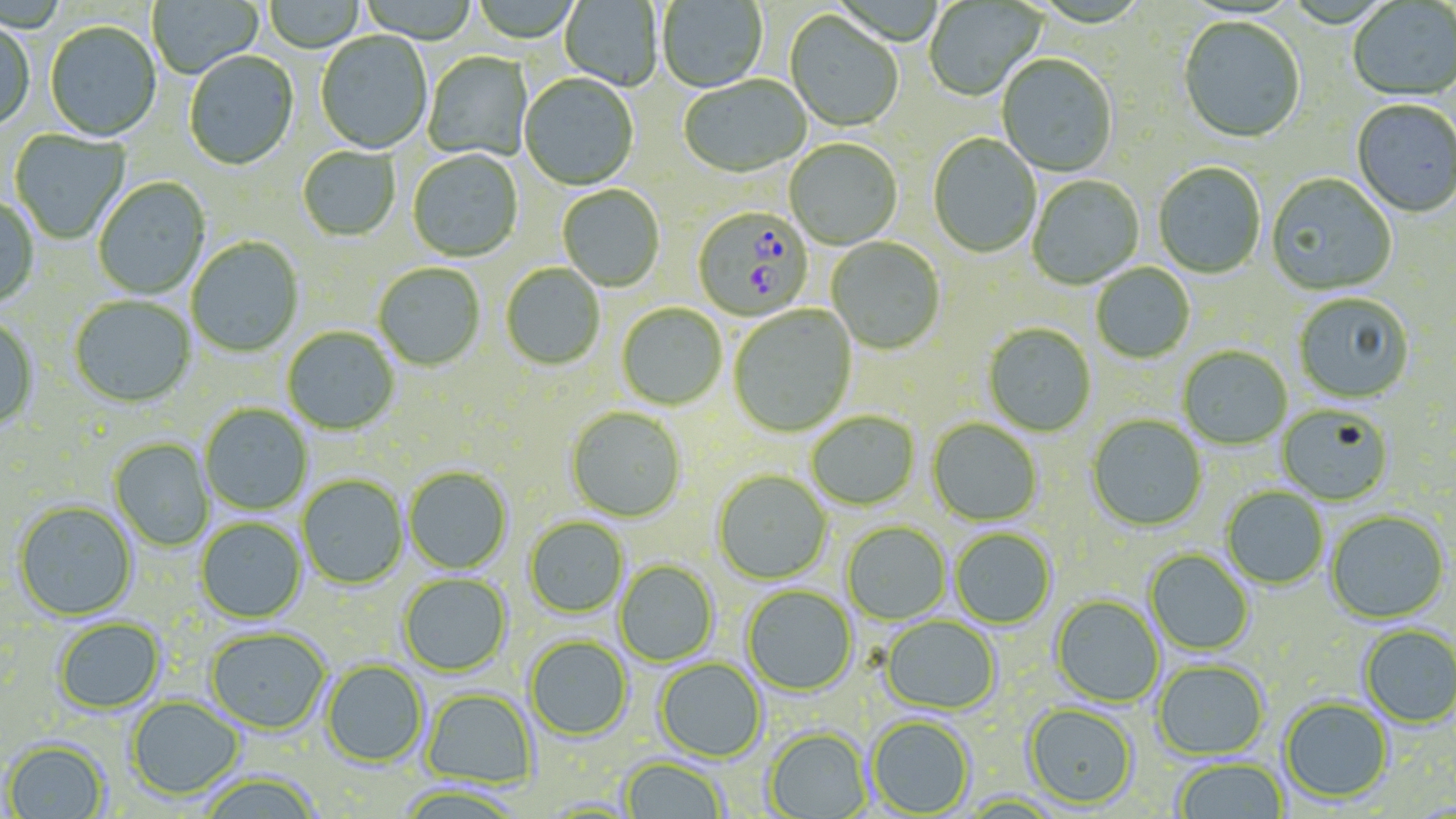
Summary:
  - Coordinate format: approximate bounding boxes as (x1,y1)-(x2,y2) corner pairs in pixels
  - Uninfected red blood cell locations: (147,0)-(263,79), (357,0)-(478,44), (470,0)-(583,44), (656,0)-(768,93), (923,0)-(1047,102), (263,1)-(365,53), (559,1)-(662,92), (1348,2)-(1456,103), (784,12)-(904,133), (1178,18)-(1306,146), (0,21)-(35,132), (44,22)-(161,143), (315,33)-(433,155), (184,52)-(299,172), (423,52)-(533,162), (996,55)-(1118,178), (519,74)-(639,191), (679,76)-(811,180), (1351,101)-(1455,219), (9,130)-(131,245), (927,134)-(1041,259), (784,140)-(903,251), (297,147)-(400,242), (407,150)-(523,263), (1153,163)-(1266,279), (1266,174)-(1397,297), (1027,175)-(1144,290), (93,177)-(210,300), (558,185)-(665,292), (0,196)-(39,309), (186,237)-(303,357), (826,238)-(945,356), (373,263)-(486,371), (500,263)-(605,370), (1090,263)-(1194,363), (1294,293)-(1414,404), (70,296)-(195,407), (616,303)-(727,410), (728,305)-(856,437), (0,316)-(39,429), (983,324)-(1096,437), (282,327)-(400,435), (1178,346)-(1292,450), (200,404)-(312,515), (1277,405)-(1393,505), (566,407)-(686,522), (807,411)-(920,510), (1087,415)-(1207,531), (928,419)-(1042,526), (110,439)-(214,552), (404,466)-(513,574), (713,469)-(832,584), (297,475)-(408,589), (1222,487)-(1329,589), (13,500)-(137,621), (1325,511)-(1449,623), (196,517)-(306,623), (524,517)-(628,618), (842,522)-(950,624), (950,528)-(1057,629), (1145,549)-(1254,655), (614,561)-(719,667), (398,573)-(511,676), (742,585)-(857,696), (1051,595)-(1164,707), (881,616)-(1001,714), (53,617)-(165,714), (1359,624)-(1456,727), (205,628)-(331,734), (525,635)-(632,741), (654,658)-(766,762), (321,660)-(428,767), (1152,660)-(1269,760), (421,688)-(538,788), (126,697)-(244,800), (1279,697)-(1393,803), (1024,703)-(1138,808), (867,715)-(975,816), (764,728)-(871,819), (3,739)-(109,819), (618,756)-(729,818), (1174,758)-(1288,818), (196,772)-(323,819), (393,783)-(529,819)
  - Plasmodium falciparum-infected red blood cell locations: (692,207)-(814,321)
  - Slide-level diagnosis: Plasmodium falciparum
  - Magnification: 1000x
  - Field of view: one of a larger specimen
  - Stain: May-Grünwald-Giemsa
  - Modality: light microscopy
  - Image size: 1456×819 pixels
  - Preparation: thin blood film